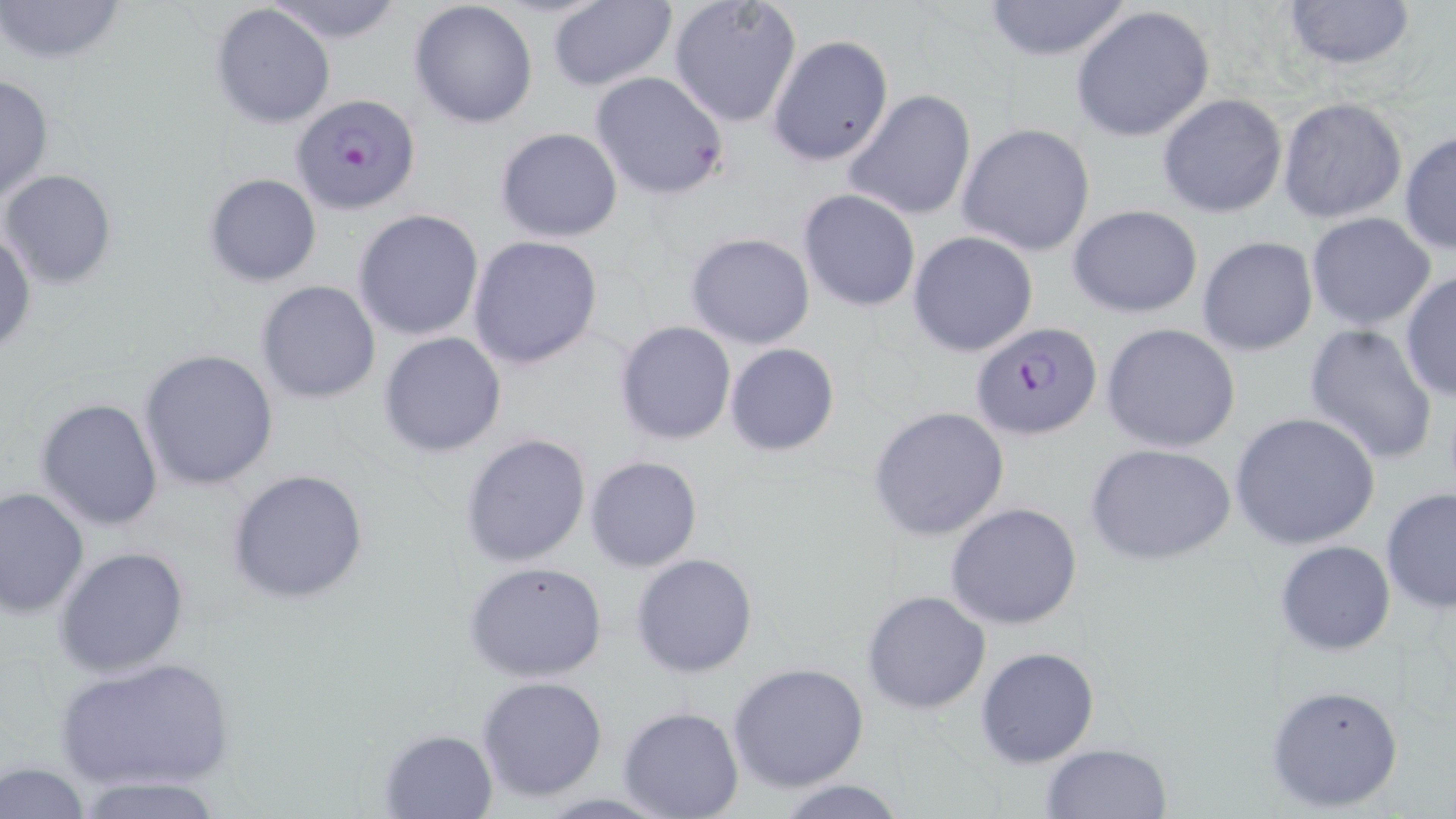

Summary:
  - Coordinate format: approximate bounding boxes as (x1, y1, x2, y2) in pixels
  - Plasmodium falciparum-infected red blood cell locations: (290, 92, 421, 214), (970, 322, 1102, 441)
  - Uninfected red blood cell locations: (0, 0, 129, 66), (668, 0, 803, 128), (980, 0, 1134, 61), (1281, 0, 1416, 71), (265, 1, 409, 44), (407, 1, 539, 130), (546, 1, 677, 92), (210, 4, 337, 130), (1070, 5, 1216, 143), (768, 34, 893, 167), (589, 71, 730, 201), (0, 72, 53, 203), (842, 90, 978, 221), (1158, 94, 1287, 217), (1277, 97, 1408, 224), (956, 123, 1096, 257), (494, 127, 623, 243), (1400, 130, 1456, 256), (1, 169, 116, 288), (204, 173, 321, 286), (797, 189, 922, 312), (1068, 204, 1203, 318), (354, 208, 485, 341), (1306, 213, 1437, 330), (0, 224, 35, 357), (907, 232, 1038, 357), (685, 233, 815, 349), (468, 236, 604, 370), (1197, 237, 1318, 356), (1399, 270, 1456, 401), (255, 280, 381, 404), (614, 320, 737, 446), (1101, 323, 1241, 453), (1304, 325, 1439, 468), (379, 332, 506, 458), (724, 343, 841, 456), (138, 349, 278, 489), (35, 397, 165, 530), (866, 405, 1010, 543), (1229, 410, 1381, 551), (459, 432, 592, 569), (1086, 443, 1236, 566), (585, 455, 703, 573), (225, 468, 370, 604), (0, 485, 89, 618), (1380, 487, 1456, 612), (945, 502, 1083, 630), (1275, 540, 1395, 656), (54, 547, 190, 678), (631, 553, 759, 678), (462, 561, 610, 682), (862, 589, 991, 715), (975, 645, 1102, 768), (56, 656, 234, 793), (728, 662, 870, 794), (476, 675, 609, 803), (1265, 682, 1403, 812), (617, 706, 745, 819), (377, 727, 498, 818), (1041, 744, 1171, 819), (1, 761, 92, 818), (69, 777, 232, 819), (769, 778, 912, 819)
  - Slide-level diagnosis: Plasmodium falciparum
  - Preparation: thin blood smear
  - Magnification: 1000x
  - Field of view: one of a larger specimen
  - Image size: 1456×819 pixels
  - Modality: optical microscopy
  - Stain: May-Grünwald-Giemsa